Assess the morphology of the erythrocytes.
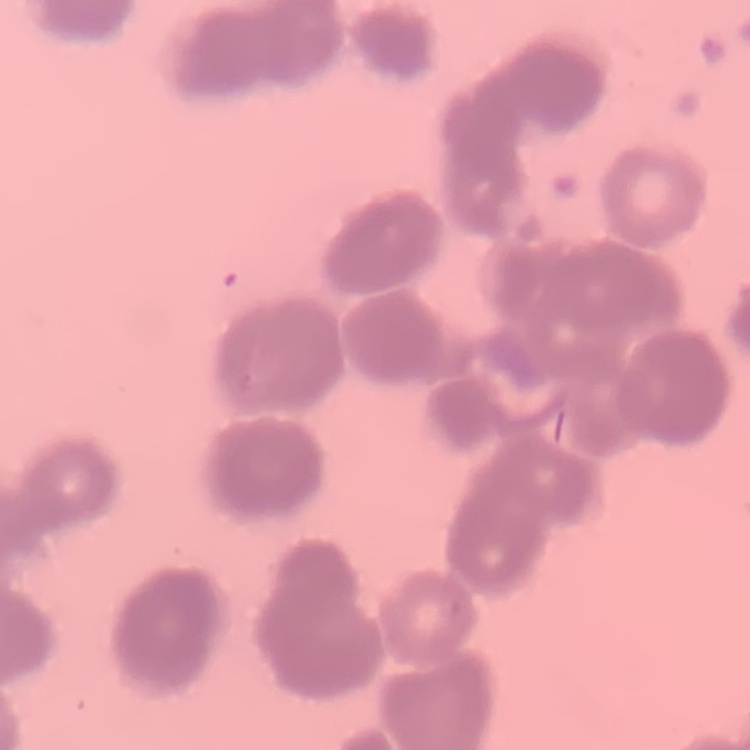
Rouleaux formation.

preparation = thin peripheral smear
image type = one tile cut from a larger photomicrograph
stain = Field's or Giemsa